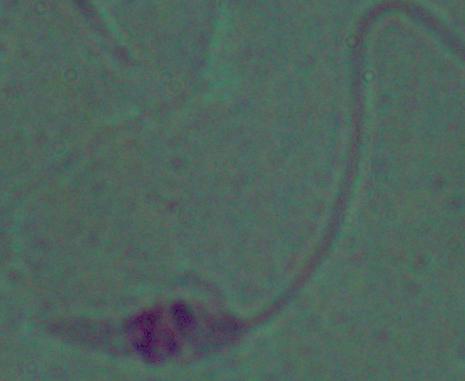
Summary:
  - Magnification: 1000x
  - Modality: micrograph
  - Identification: Leishmania